Assess this cell for malaria.
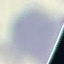
Uninfected.

Acquired by smartphone through the microscope eyepiece. Automatically extracted cell patch, resized to 64 × 64 pixels. Giemsa-stained preparation. Thin blood smear.